Report the malaria status.
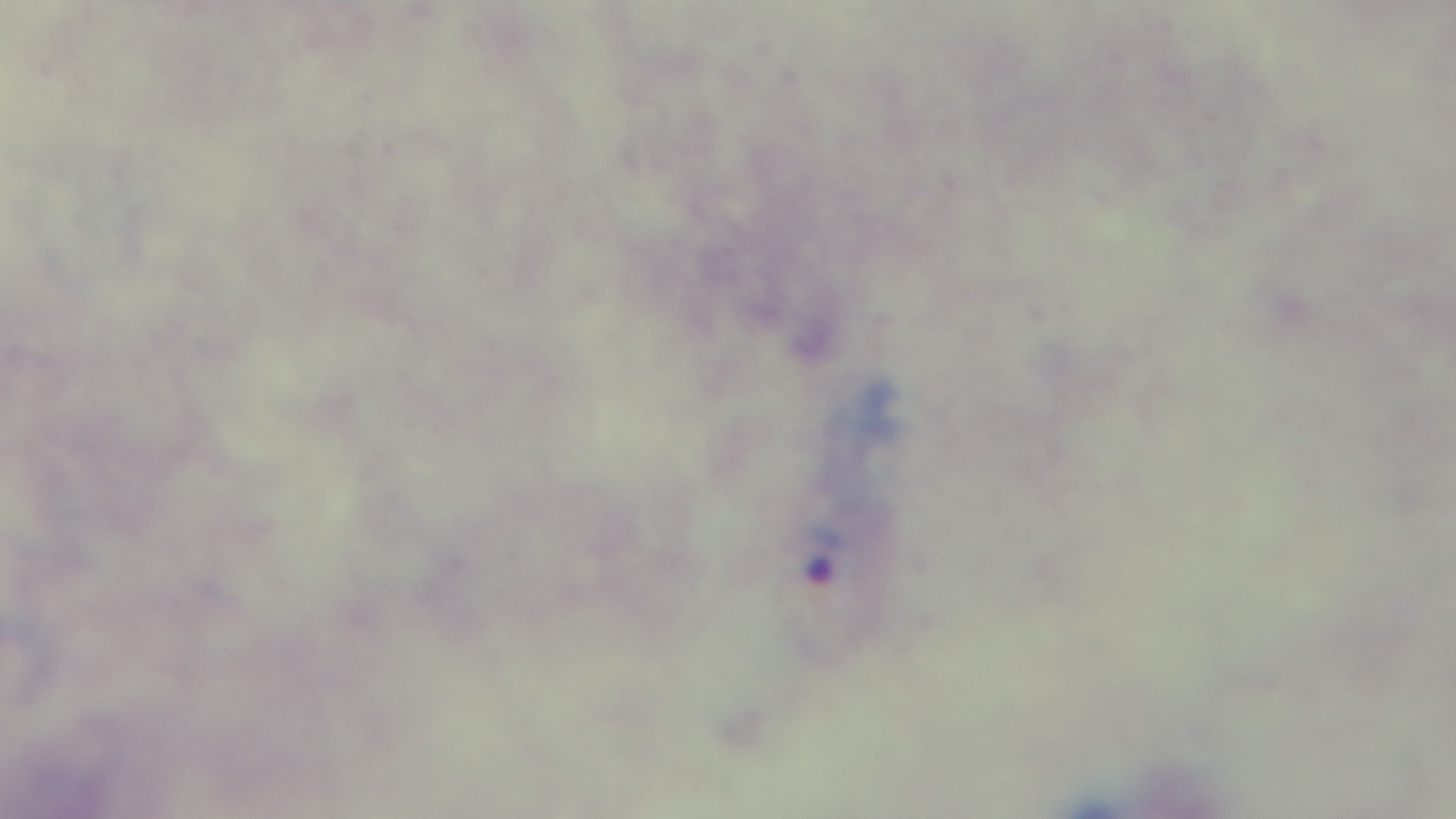

Infected.

Mounted 4K digital camera. Preparation: thick smear. Light microscopy. Giemsa stain. Oil-immersion objective, 100x. One field from the slide.